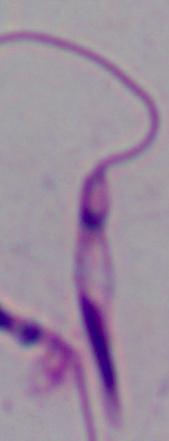

Summary:
  - Magnification: 1000x
  - Identification: Leishmania
  - Modality: micrograph